Identify the parasite.
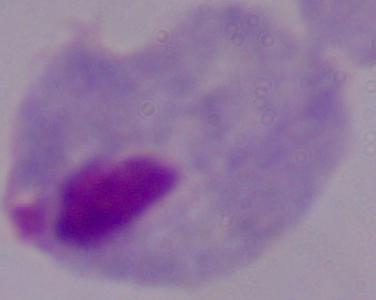

A trichomonad.

Captured at 1000x magnification. Micrograph.